State the blood parasite species.
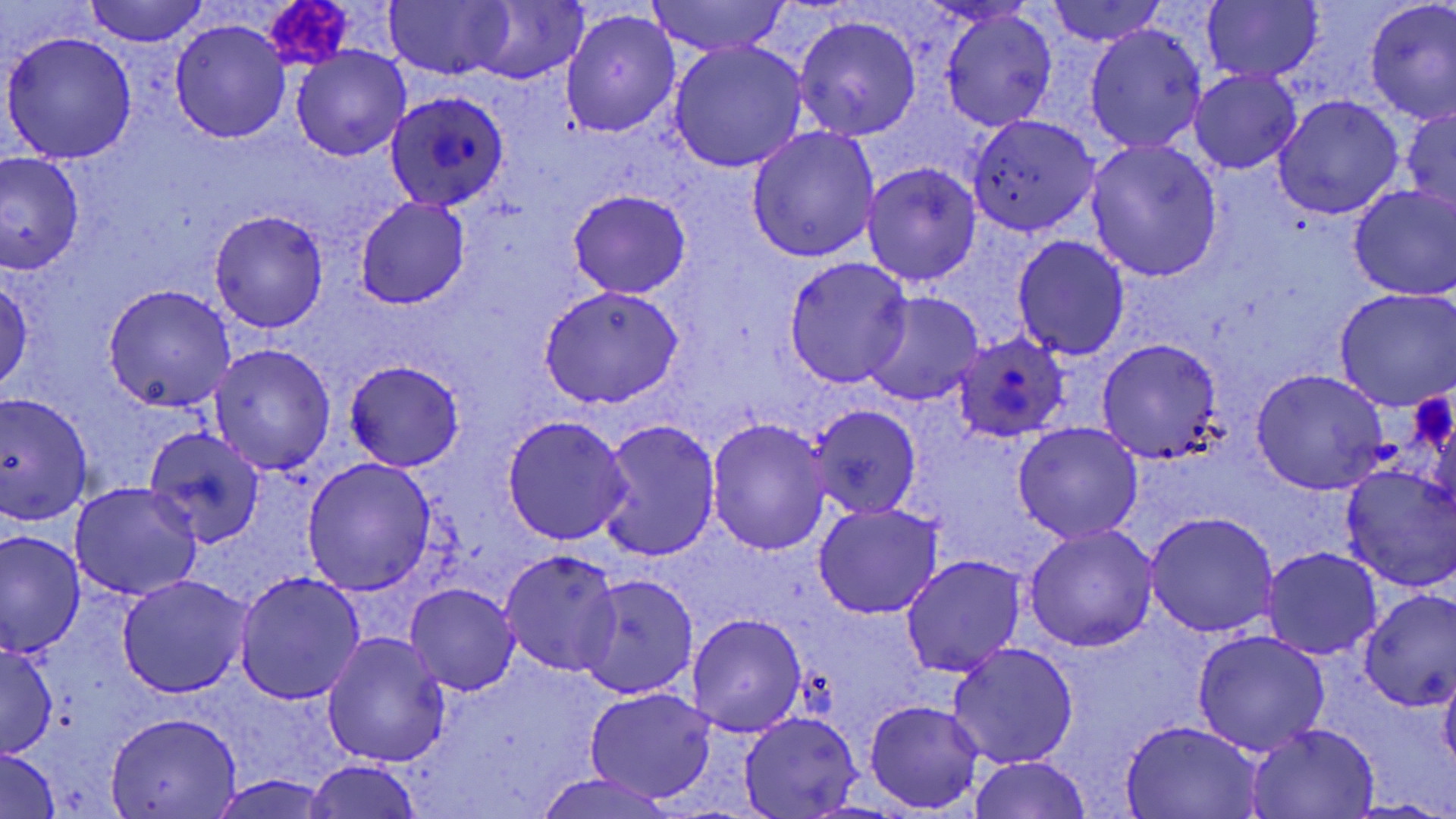

Plasmodium ovale.

field_of_view: single
plasmodium_ovale_infected_red_blood_cell_locations: 'approximate bounding boxes as (x1,y1)-(x2,y2) corner pairs in pixels: (385,86)-(509,209), (956,333)-(1069,443)'
platelet_locations: 'approximate bounding boxes as (x1,y1)-(x2,y2) corner pairs in pixels: (265,2)-(353,69), (1409,392)-(1456,459)'
modality: optical microscopy
image_size: 1456×819 pixels
magnification: 1000x
preparation: thin blood smear
stain: May-Grünwald-Giemsa
uninfected_red_blood_cell_locations: 'approximate bounding boxes as (x1,y1)-(x2,y2) corner pairs in pixels: (86,0)-(207,46), (645,0)-(794,57), (1045,0)-(1166,47), (1364,0)-(1456,122), (382,1)-(514,80), (466,1)-(586,84), (1201,2)-(1323,84), (940,8)-(1056,131), (561,9)-(681,138), (792,15)-(921,140), (170,19)-(290,143), (1086,24)-(1206,154), (3,30)-(137,163), (670,43)-(807,171), (290,46)-(410,162), (1191,71)-(1301,174), (1272,95)-(1404,218), (1401,107)-(1456,213), (966,113)-(1101,237), (746,126)-(881,262), (1087,138)-(1223,282), (2,153)-(84,273), (862,163)-(981,287), (1349,183)-(1456,301), (567,189)-(691,299), (354,197)-(471,309), (210,209)-(328,332), (1012,236)-(1130,360), (783,256)-(912,388), (1,275)-(32,393), (102,285)-(239,411), (539,286)-(684,407), (1334,289)-(1455,410), (862,291)-(985,407), (1098,337)-(1224,463), (209,343)-(335,473), (345,360)-(463,470), (1251,370)-(1388,494), (0,392)-(94,523), (808,404)-(922,520), (501,415)-(632,545), (597,419)-(720,562), (705,419)-(830,558), (1013,422)-(1143,544), (145,425)-(267,548), (303,459)-(435,594), (1338,463)-(1456,591), (69,483)-(202,601), (813,503)-(942,618), (1143,514)-(1278,637), (1024,525)-(1157,651), (1,533)-(84,657), (1261,546)-(1384,660), (500,552)-(623,675), (900,556)-(1026,677), (233,571)-(366,705), (579,574)-(697,699), (117,576)-(253,696), (406,582)-(519,694), (1359,590)-(1456,708), (687,613)-(807,738), (1191,630)-(1330,756), (322,632)-(452,768), (0,642)-(57,758), (948,643)-(1079,770), (1439,665)-(1456,772), (585,688)-(714,803), (864,700)-(986,814), (739,711)-(862,818), (104,713)-(242,818), (1120,719)-(1263,818), (1245,723)-(1381,817), (0,748)-(60,819), (966,756)-(1093,819), (305,760)-(423,819), (533,771)-(679,818), (209,774)-(335,818), (1343,799)-(1450,817)'